Give the position of every leukocyte visible.
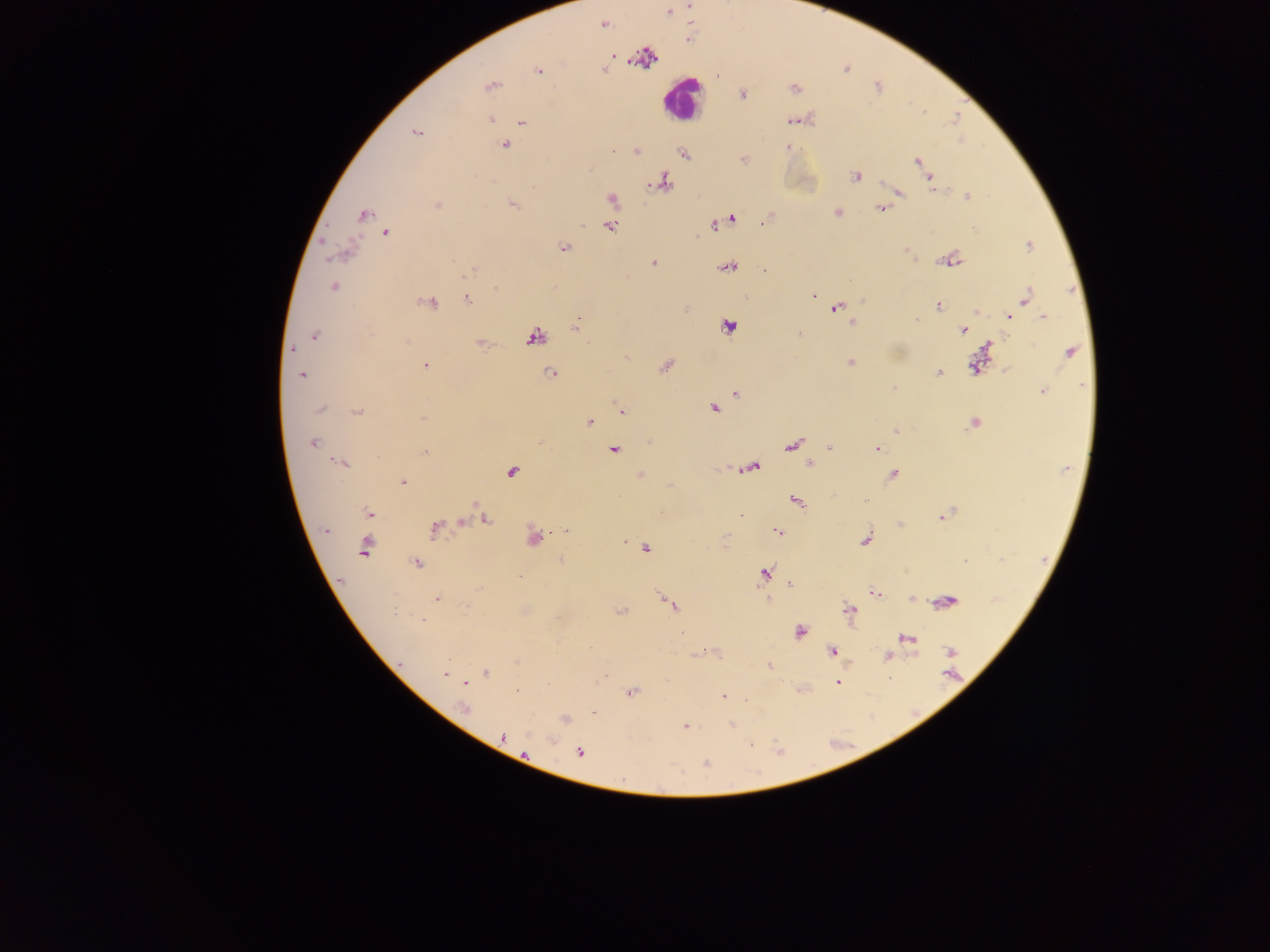
Approximate centers as (x, y) in pixels.
Leukocytes: (679, 98).

country = Ghana
capture = mobile-phone photograph through a microscope
preparation = thick blood film
field of view = single
malaria parasite locations = approximate centers as (x, y) in pixels: (669, 13), (603, 24), (538, 71), (490, 86), (742, 94), (491, 120), (790, 120), (521, 122), (416, 132), (505, 145), (788, 147), (613, 151), (636, 151), (683, 153), (743, 160), (916, 161), (855, 176), (931, 181), (663, 182), (900, 192), (968, 197), (612, 199), (513, 205), (438, 206), (880, 208), (837, 212), (364, 215), (733, 218), (765, 222), (714, 226), (610, 227), (386, 233), (1028, 246), (564, 247), (952, 260), (653, 263), (728, 267), (764, 271), (470, 272), (334, 287), (496, 289), (812, 295), (1025, 298), (468, 300), (428, 302), (938, 306), (836, 308), (977, 311), (1009, 317), (1043, 317), (916, 320), (578, 321), (853, 323), (727, 326), (963, 331), (799, 334), (315, 335), (535, 337), (407, 341), (482, 344), (293, 349), (1069, 353), (851, 363), (425, 365), (974, 365), (666, 366), (939, 373), (550, 374), (302, 375), (893, 388), (1042, 391), (736, 393), (713, 409), (319, 410), (621, 411), (356, 412), (423, 418), (589, 422), (973, 423), (895, 430), (312, 443), (792, 446), (829, 447), (876, 448), (615, 450), (425, 453), (341, 463), (810, 464), (752, 467), (512, 471), (893, 474), (639, 476), (402, 482), (866, 500), (796, 501), (368, 513), (941, 516), (487, 519), (435, 528), (325, 530), (778, 531), (564, 532), (534, 538), (866, 539), (625, 542), (365, 549), (646, 549), (561, 560), (965, 561), (416, 563), (764, 573), (519, 577), (791, 584), (874, 593), (436, 599), (768, 599), (949, 600), (671, 605), (849, 609), (395, 610), (621, 612), (422, 619), (800, 632), (906, 638), (707, 651), (833, 652), (950, 652), (887, 657), (517, 661), (769, 666), (487, 673), (445, 674), (465, 683), (837, 683), (517, 691), (631, 692), (724, 696), (465, 708), (593, 712), (565, 720), (732, 724), (685, 727), (503, 738), (552, 740), (751, 745), (580, 753), (525, 754), (706, 763)
image size = 1270×952 pixels